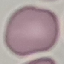

malaria_status: uninfected
capture: smartphone camera at the microscope eyepiece
stain: Giemsa
preparation: thin blood film
image_type: cell patch, automatically extracted from a larger field of view and resized to 64 × 64 pixels